Identify the parasite.
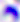

This is Toxoplasma gondii.

Summary:
  - Modality: photomicrograph
  - Magnification: 400x